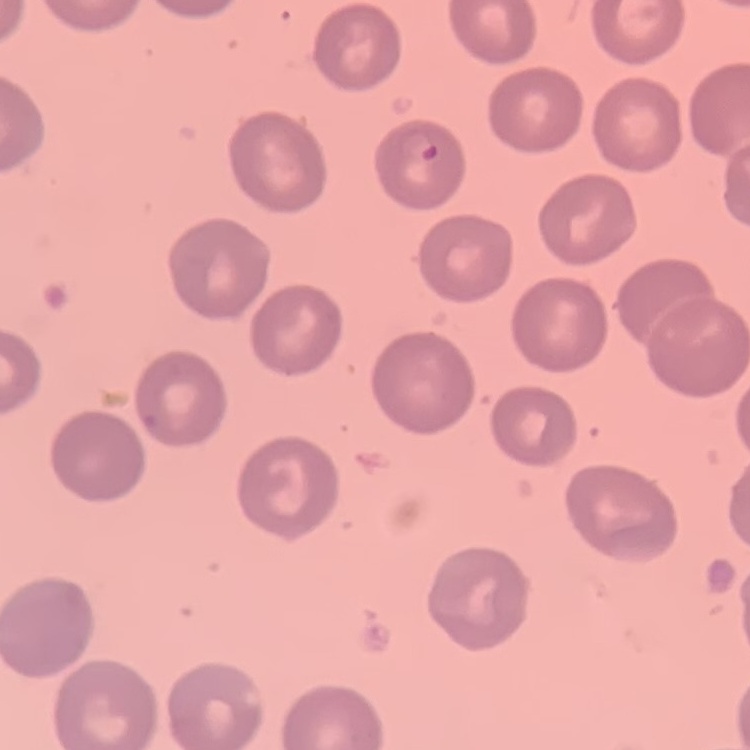 The erythrocytes exhibit no rouleaux formation. Thin blood smear. Square crop of a larger photomicrograph. Field's or Giemsa stain.